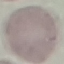

Summary:
  - Malaria status: uninfected
  - Stain: Giemsa
  - Preparation: thin smear
  - Capture: smartphone through the microscope eyepiece
  - Image type: automatically extracted cell patch, resized to 64 × 64 pixels